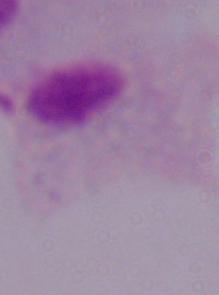
1000x magnification. A trichomonad is seen. Photomicrograph.